Locate every uninfected red blood cell.
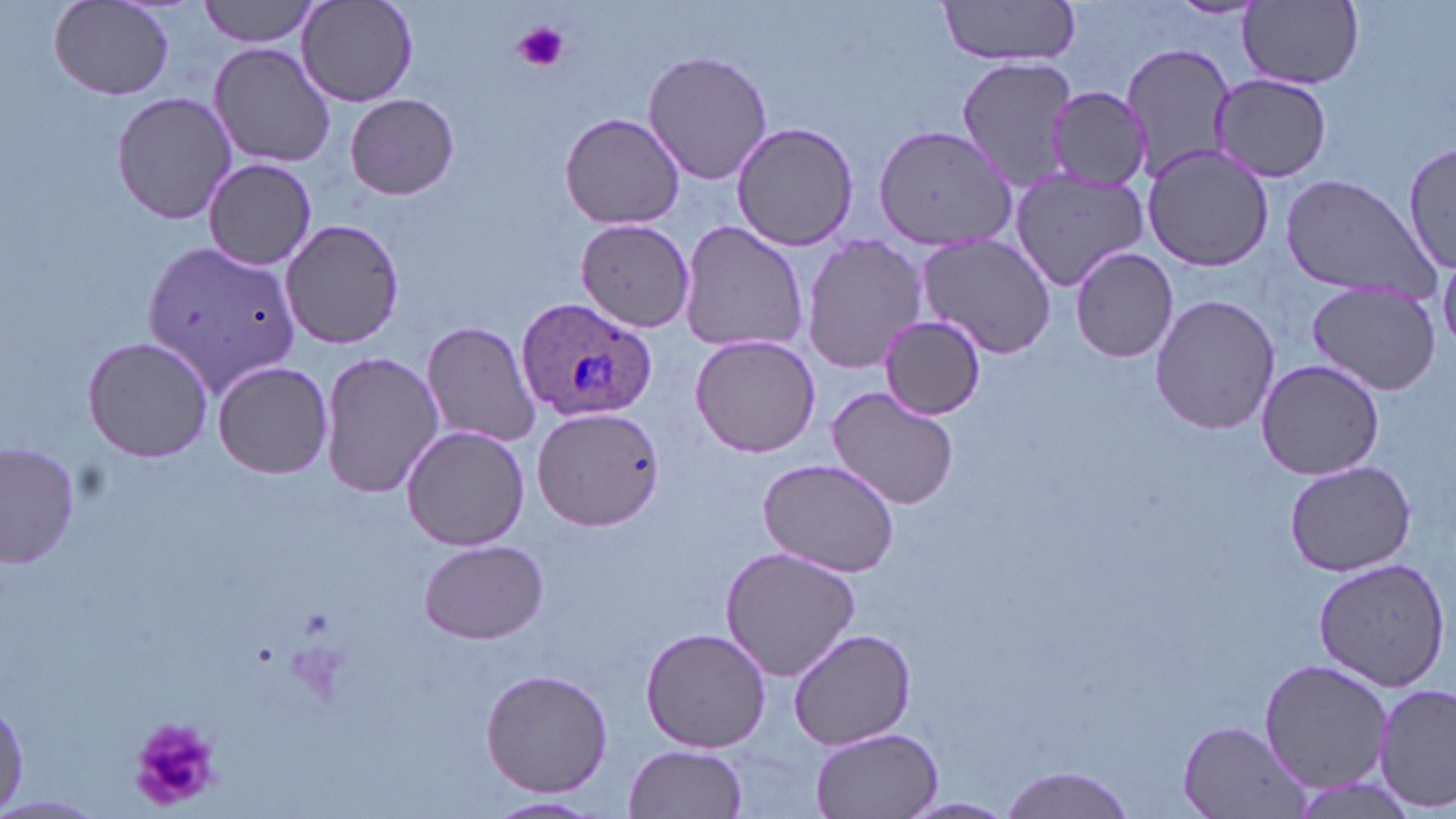

Approximate bounding boxes as (x1,y1)-(x2,y2) corner pairs in pixels.
Uninfected red blood cells: (199,0)-(326,47), (935,0)-(1084,66), (298,1)-(418,108), (50,2)-(175,100), (1238,2)-(1365,89), (1122,41)-(1237,180), (209,42)-(336,169), (643,49)-(772,186), (954,56)-(1077,192), (1210,73)-(1332,182), (1048,86)-(1151,195), (111,92)-(236,224), (346,93)-(459,201), (560,112)-(686,230), (729,122)-(859,250), (870,124)-(1012,252), (1402,136)-(1454,278), (1142,145)-(1277,272), (204,158)-(317,269), (1009,167)-(1148,290), (1279,173)-(1438,300), (280,217)-(406,351), (573,218)-(696,333), (678,220)-(810,357), (916,232)-(1060,360), (801,235)-(928,375), (142,238)-(300,397), (1069,245)-(1179,364), (1306,283)-(1441,396), (1148,293)-(1281,436), (877,315)-(987,419), (422,320)-(544,447), (689,334)-(824,459), (82,336)-(215,464), (319,350)-(443,500), (1254,358)-(1386,480), (211,360)-(334,479), (827,386)-(959,509), (532,406)-(664,530), (401,424)-(530,551), (2,440)-(81,571), (755,458)-(903,578), (1282,461)-(1417,578), (417,539)-(549,644), (718,545)-(862,683), (1312,559)-(1448,690), (640,626)-(772,753), (786,628)-(915,751), (1259,658)-(1391,795), (480,669)-(613,798), (1375,683)-(1455,812), (1177,720)-(1312,818), (809,728)-(943,818), (624,743)-(749,819), (993,767)-(1139,819), (0,793)-(105,817), (483,794)-(604,817), (896,798)-(1024,818).

Summary:
  - Platelet locations: (514,21)-(570,74), (126,714)-(224,814)
  - Plasmodium ovale-infected red blood cell locations: (514,296)-(660,427)
  - Slide-level diagnosis: Plasmodium ovale
  - Preparation: thin blood smear
  - Image size: 1456×819 pixels
  - Modality: light microscopy
  - Field of view: one of a larger specimen
  - Magnification: 1000x
  - Stain: May-Grünwald-Giemsa